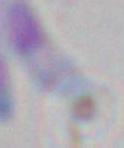 Toxoplasma gondii is shown. 1000x magnification. Photomicrograph.